Comment on the morphology of the red blood cells.
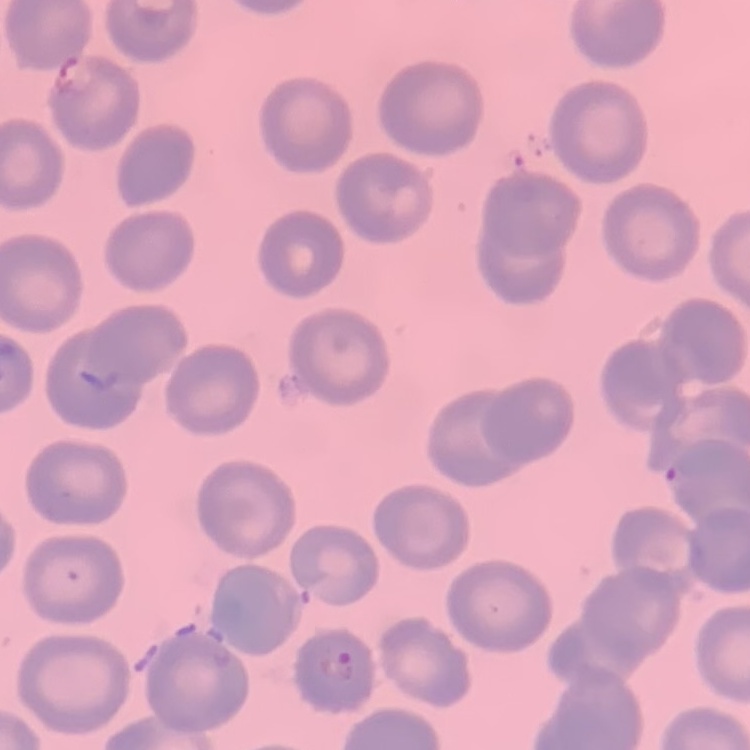
They show no rouleaux formation.

Stained with either Field's or Giemsa. One tile cut from a larger photomicrograph. Thin peripheral smear.